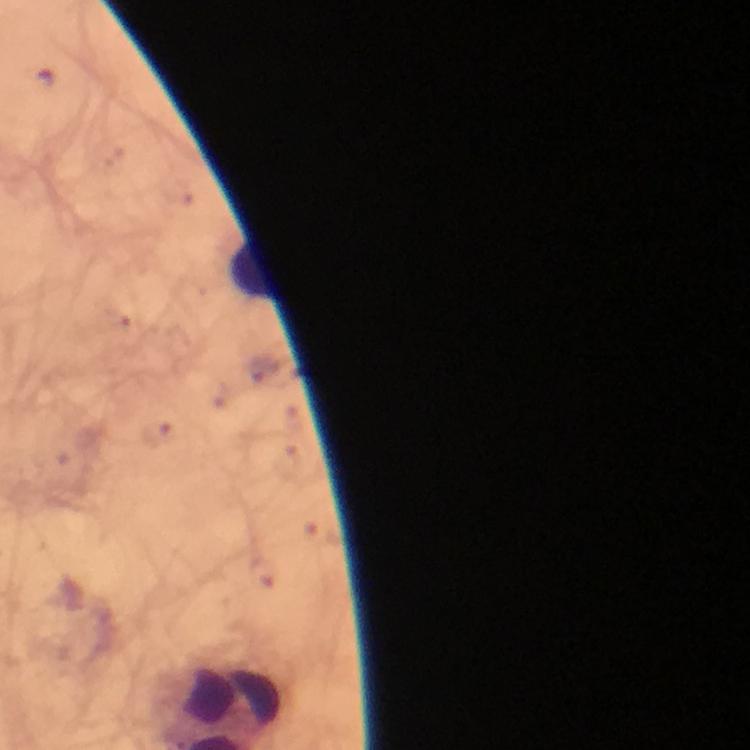
Approximate centers as [x, y] in pixels.
Summary:
  - Leukocyte locations: [252, 268]
  - Magnification: 100x
  - Plasmodium parasites: none seen
  - Capture: smartphone photograph through a microscope
  - Immersion oil: applied
  - Preparation: thick blood film
  - Image size: 750×750 pixels
  - Cropped from: a single field of view
  - Context: from a diagnostic examination for malaria
  - Stain: Giemsa